Describe the morphology of the erythrocytes.
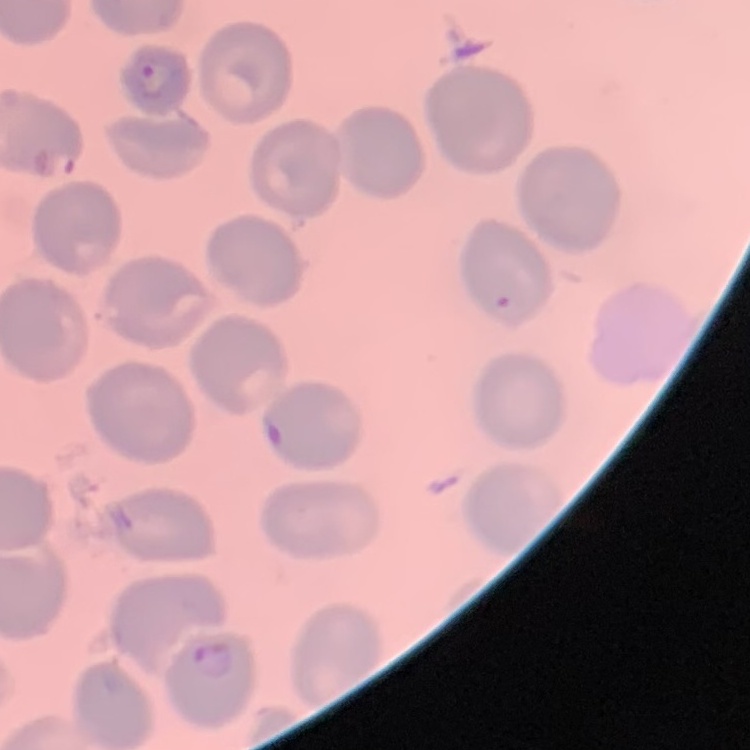

No rouleaux formation.

preparation = thin peripheral smear
image type = one tile cut from a larger photomicrograph
stain = Field's or Giemsa